Report the malaria status of this cell.
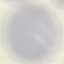

It is uninfected.

Automatically extracted cell patch, resized to 64 × 64 pixels. Thin blood smear. Photographed with a smartphone camera at the microscope eyepiece. Giemsa stain.